Give the position of every Plasmodium parasite visible.
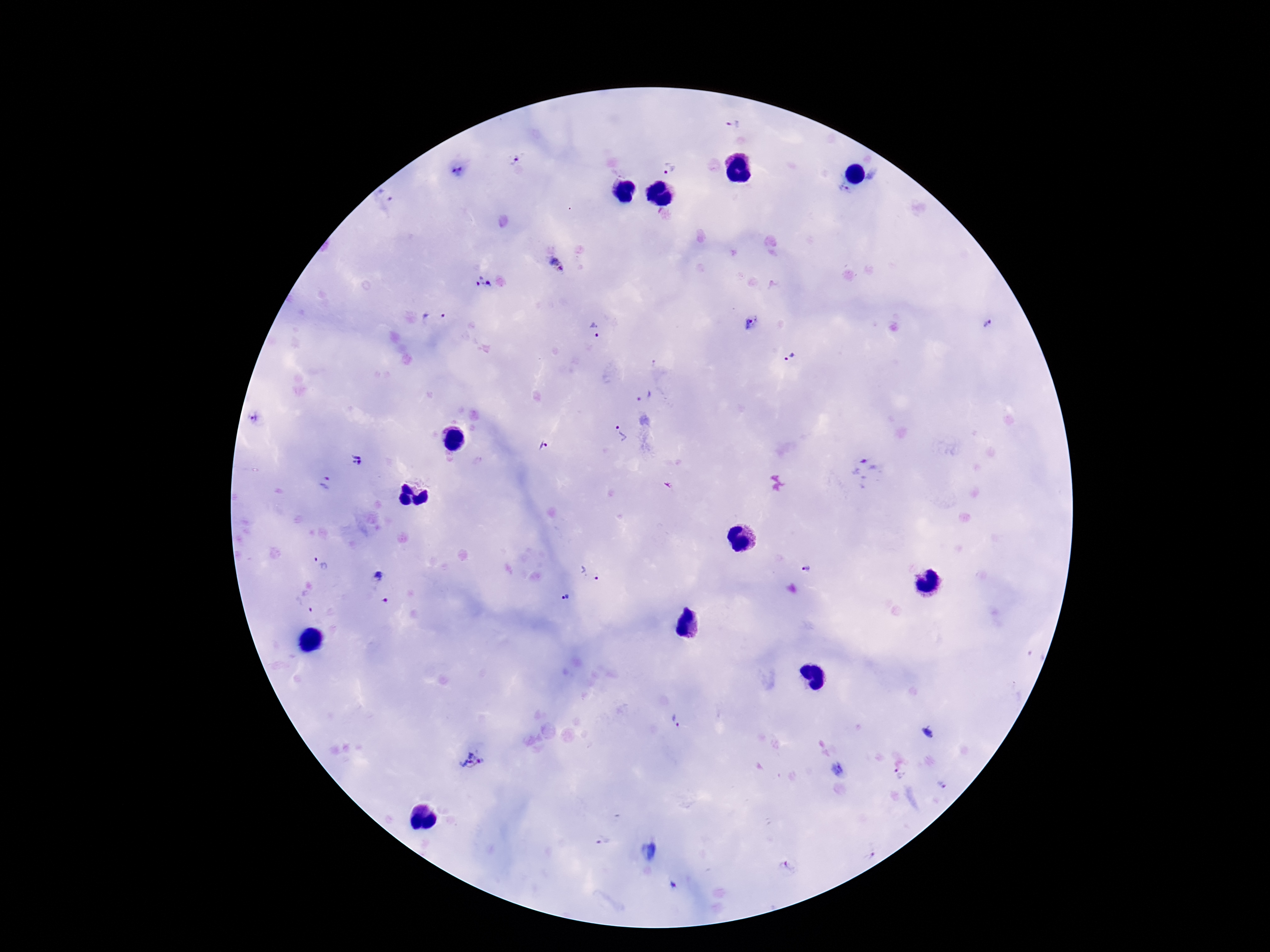

Approximate centers as [x, y] in pixels.
Plasmodium parasites: [733, 126], [512, 158], [668, 167], [457, 172], [844, 189], [386, 194], [558, 265], [482, 283], [433, 316], [987, 322], [751, 323], [596, 330], [790, 357], [654, 363], [644, 395], [255, 419], [619, 435], [542, 446], [357, 461], [864, 472], [325, 483], [321, 563], [805, 570], [592, 572], [379, 576], [564, 599], [304, 606], [676, 721], [927, 732], [472, 762], [899, 774], [942, 785], [603, 842], [870, 857], [789, 867].

Summary:
  - Field of view: one from this slide
  - Image size: 1270×952 pixels
  - Stain: Giemsa
  - Magnification: 100x
  - Preparation: thick blood film
  - Capture: smartphone camera through the microscope eyepiece
  - Patient malaria status: infected